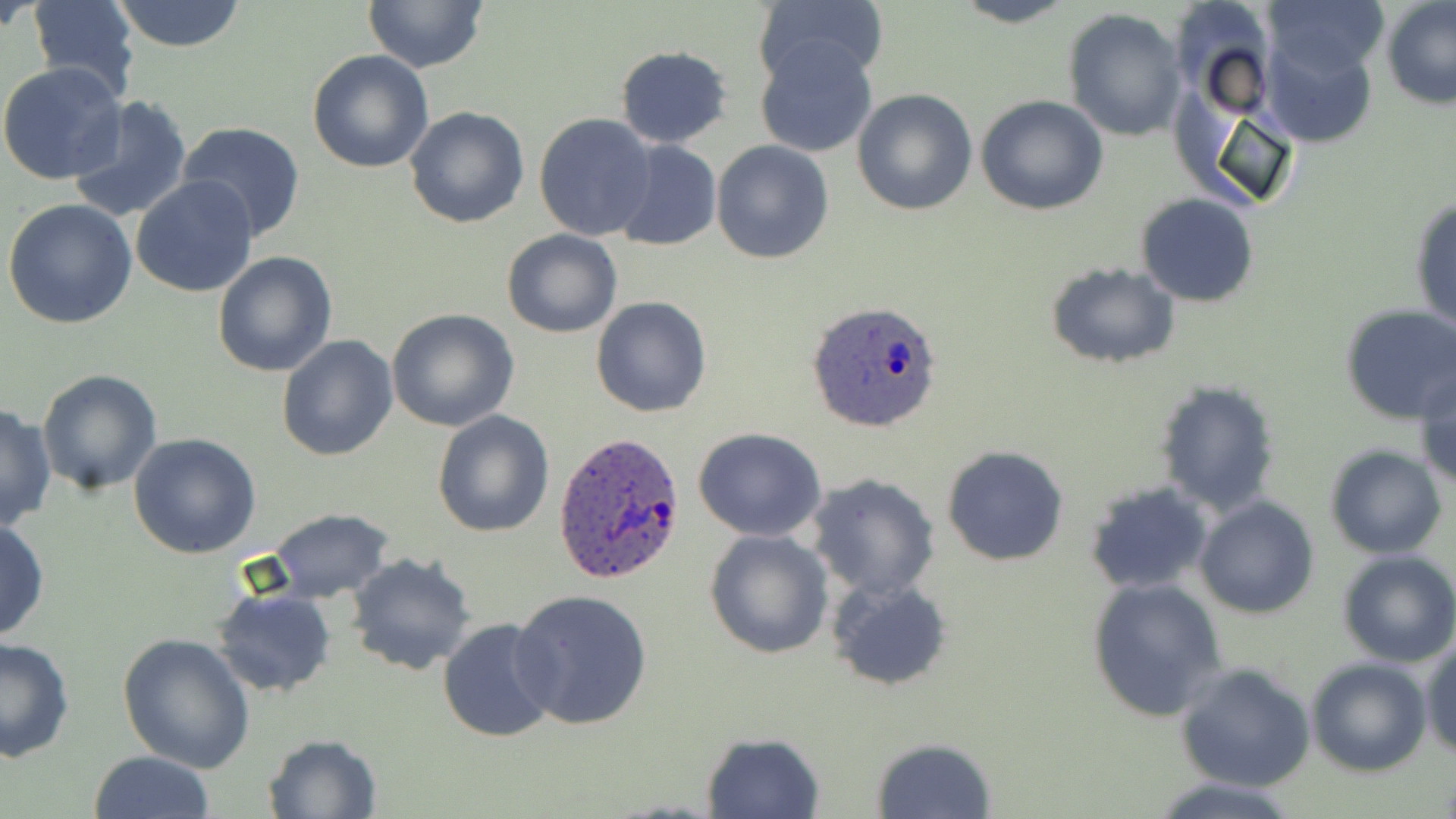
slide-level diagnosis = Plasmodium ovale
modality = light microscopy
magnification = 1000x
preparation = thin blood film
uninfected red blood cell locations = approximate bounding boxes as (x1,y1)-(x2,y2) corner pairs in pixels: (26,0)-(142,98), (110,0)-(248,51), (950,0)-(1079,27), (1266,0)-(1388,78), (1383,0)-(1456,108), (365,1)-(488,72), (753,1)-(887,86), (1062,8)-(1187,142), (1257,22)-(1382,149), (754,37)-(879,159), (616,45)-(732,148), (307,49)-(434,173), (0,61)-(128,186), (851,88)-(978,216), (976,94)-(1108,216), (67,95)-(192,223), (405,106)-(529,228), (533,114)-(658,241), (178,122)-(306,242), (611,140)-(722,253), (710,140)-(835,264), (131,173)-(259,298), (1135,193)-(1259,306), (1409,195)-(1456,331), (3,198)-(137,329), (502,229)-(622,339), (213,250)-(339,377), (1044,261)-(1181,368), (591,297)-(712,418), (1339,305)-(1456,425), (386,308)-(519,431), (275,335)-(398,461), (1413,359)-(1456,489), (37,370)-(163,495), (1154,379)-(1281,516), (0,403)-(55,532), (433,408)-(556,538), (693,427)-(827,543), (129,433)-(260,558), (1324,444)-(1447,559), (942,445)-(1070,566), (805,473)-(940,600), (1085,481)-(1214,595), (1195,495)-(1319,619), (267,508)-(394,601), (0,519)-(49,643), (703,529)-(834,660), (1336,550)-(1456,666), (346,552)-(479,676), (827,575)-(954,690), (1087,578)-(1228,723), (212,588)-(337,697), (510,588)-(657,731), (438,617)-(562,741), (116,633)-(257,774), (0,634)-(75,763), (1422,637)-(1455,758), (1305,657)-(1431,776), (1174,662)-(1317,791), (700,732)-(824,819), (262,734)-(384,818), (870,737)-(996,818), (88,750)-(217,819), (1150,776)-(1301,819)
image size = 1456×819 pixels
field of view = single
stain = May-Grünwald-Giemsa
Plasmodium ovale-infected red blood cell locations = approximate bounding boxes as (x1,y1)-(x2,y2) corner pairs in pixels: (807,300)-(943,434), (552,432)-(690,586)